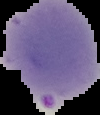

image size = 100×115 pixels
preparation = thin blood film
image type = segmented cell region with the area outside set to black
result = malaria parasites identified